Give a bounding box for every Plasmodium parasite.
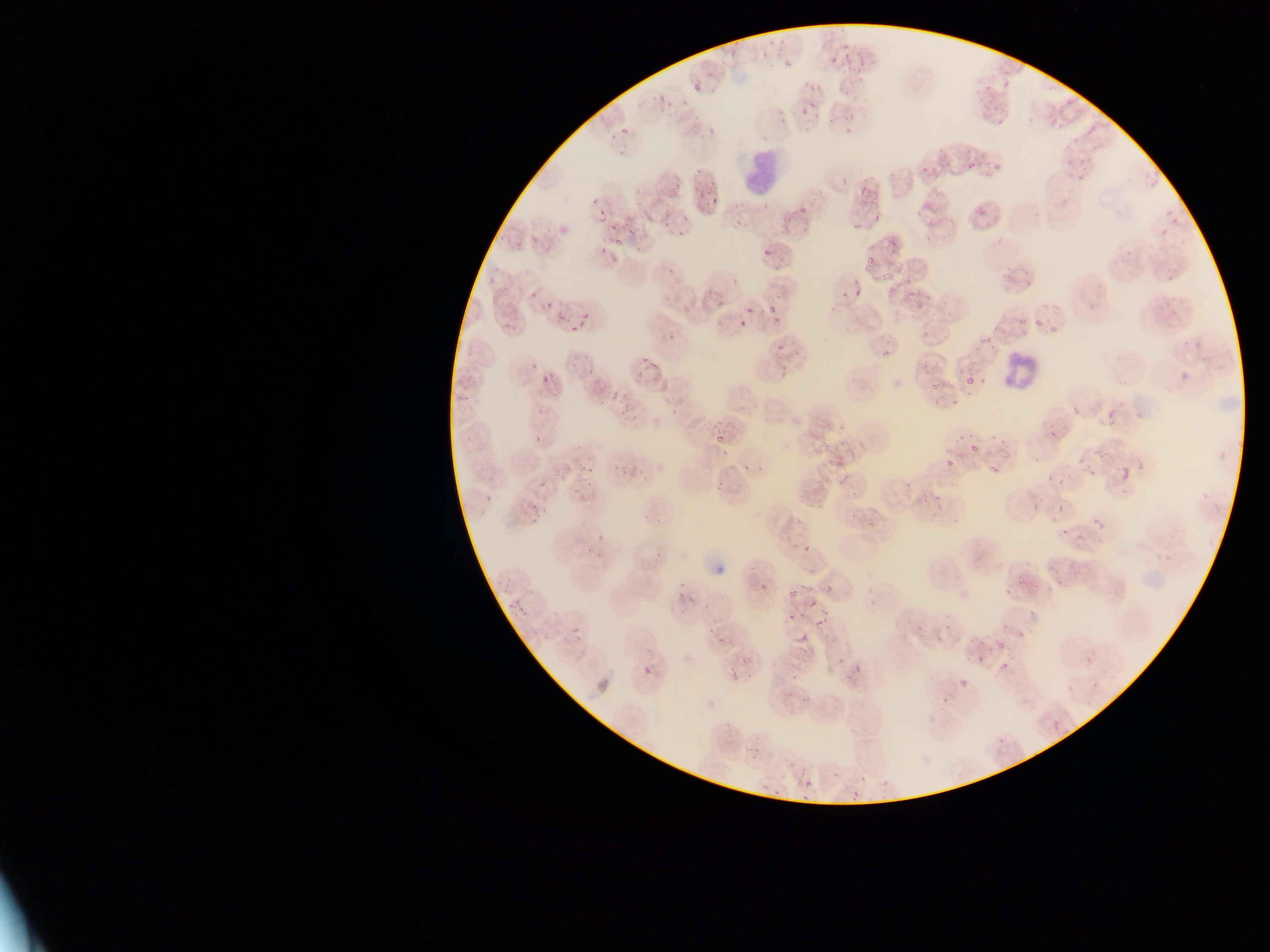

Approximate bounding boxes as {left, top, right, bottom} in pixels.
Plasmodium parasites: {619, 126, 629, 136}, {1087, 127, 1094, 135}, {918, 150, 946, 176}, {981, 159, 1009, 180}, {968, 162, 977, 171}, {657, 167, 691, 209}, {694, 167, 704, 175}, {1074, 171, 1089, 185}, {1145, 172, 1159, 191}, {856, 182, 870, 201}, {699, 191, 719, 208}, {973, 195, 991, 221}, {792, 203, 809, 220}, {1159, 203, 1172, 218}, {597, 206, 607, 221}, {673, 211, 703, 239}, {869, 211, 887, 228}, {1166, 213, 1186, 226}, {664, 214, 676, 227}, {608, 218, 632, 244}, {1154, 228, 1163, 240}, {881, 229, 902, 257}, {512, 230, 526, 250}, {539, 235, 556, 252}, {759, 241, 771, 256}, {861, 248, 882, 276}, {663, 264, 683, 283}, {481, 270, 500, 297}, {701, 279, 722, 306}, {849, 279, 869, 300}, {883, 279, 897, 296}, {529, 286, 555, 309}, {832, 286, 850, 299}, {906, 289, 920, 309}, {766, 293, 782, 324}, {660, 294, 676, 306}, {733, 297, 759, 331}, {577, 303, 600, 321}, {825, 303, 839, 316}, {555, 307, 567, 322}, {1027, 314, 1051, 337}, {570, 322, 580, 330}, {972, 323, 993, 351}, {666, 327, 676, 340}, {917, 330, 936, 346}, {875, 342, 890, 359}, {769, 344, 782, 356}, {635, 352, 658, 378}, {1177, 363, 1192, 383}, {775, 364, 789, 378}, {537, 367, 560, 393}, {599, 369, 626, 408}, {959, 372, 985, 390}, {658, 381, 668, 394}, {929, 381, 938, 390}, {619, 382, 639, 407}, {661, 384, 680, 409}, {948, 388, 959, 406}, {1070, 402, 1082, 418}, {535, 404, 548, 417}, {1101, 407, 1113, 424}, {711, 418, 732, 452}, {1044, 423, 1059, 440}, {531, 429, 544, 443}, {814, 434, 837, 459}, {734, 440, 761, 471}, {963, 440, 978, 454}, {572, 442, 601, 494}, {943, 443, 966, 468}, {984, 450, 1013, 483}, {627, 451, 657, 474}, {612, 462, 622, 476}, {835, 462, 852, 482}, {1119, 467, 1129, 480}, {1087, 468, 1096, 478}, {1047, 475, 1055, 483}, {538, 478, 548, 489}, {1045, 497, 1068, 515}, {846, 505, 867, 534}, {1055, 515, 1076, 539}, {1089, 515, 1105, 528}, {802, 544, 810, 553}, {751, 573, 778, 599}, {996, 574, 1022, 600}, {671, 576, 697, 600}, {1049, 578, 1066, 594}, {786, 579, 807, 601}, {819, 581, 840, 604}, {805, 600, 832, 625}, {780, 609, 800, 627}, {706, 611, 721, 634}, {935, 619, 951, 640}, {570, 625, 583, 639}, {798, 631, 809, 643}, {995, 632, 1017, 662}, {972, 645, 987, 670}, {994, 646, 1015, 675}, {1084, 654, 1093, 665}, {837, 657, 845, 666}, {733, 658, 753, 680}, {847, 662, 868, 695}, {953, 670, 971, 685}, {1066, 683, 1073, 691}, {794, 687, 811, 709}, {1051, 721, 1060, 730}, {804, 778, 812, 787}, {842, 780, 863, 806}.

{
  "field_of_view": "single",
  "image_size": "1270×952 pixels",
  "country": "Ghana",
  "capture": "mobile-phone photograph through a microscope",
  "leukocyte_locations": "approximate bounding boxes as {left, top, right, bottom} in pixels: {738, 133, 776, 205}, {1002, 349, 1035, 389}",
  "preparation": "thin blood smear"
}